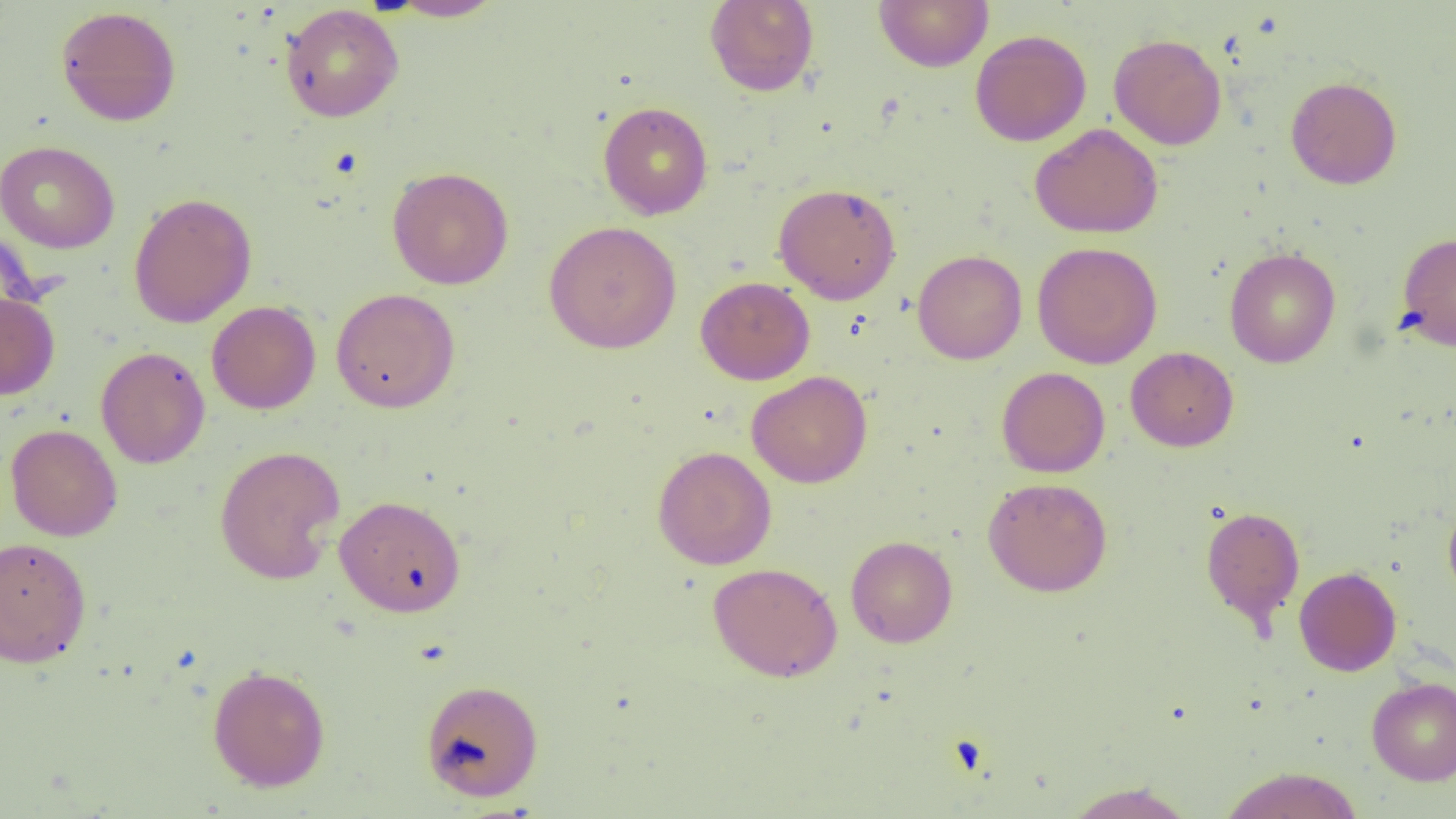 Approximate bounding boxes as (x1, y1, x2, y2) in pixels. Uninfected red blood cell locations: (874, 0, 993, 72), (385, 1, 505, 22), (704, 1, 819, 97), (280, 4, 404, 122), (55, 6, 182, 126), (970, 29, 1091, 147), (1108, 33, 1227, 150), (1286, 76, 1402, 189), (598, 101, 713, 220), (1030, 123, 1163, 238), (0, 140, 120, 253), (387, 166, 514, 290), (773, 183, 901, 305), (128, 192, 257, 328), (543, 221, 682, 354), (1396, 231, 1456, 351), (1032, 242, 1162, 368), (1224, 247, 1340, 368), (912, 249, 1026, 364), (696, 276, 815, 385), (331, 288, 460, 413), (0, 292, 60, 399), (206, 300, 321, 414), (1126, 346, 1239, 452), (96, 347, 210, 469), (996, 367, 1110, 478), (747, 371, 872, 488), (5, 424, 122, 541), (214, 444, 346, 585), (652, 445, 776, 570), (983, 477, 1112, 596), (334, 495, 466, 617), (1443, 500, 1456, 604), (1200, 505, 1305, 629), (0, 535, 92, 668), (846, 536, 957, 647), (707, 562, 843, 682), (1294, 566, 1402, 676), (207, 664, 331, 792), (1366, 677, 1456, 785), (420, 678, 544, 801), (1218, 767, 1364, 818), (1062, 781, 1196, 819). Slide-level diagnosis: no evidence of blood parasites. Single field of view. Thin blood film. Image is 1456×819 pixels. 1000x magnification. Light microscopy.